Name the blood parasite species.
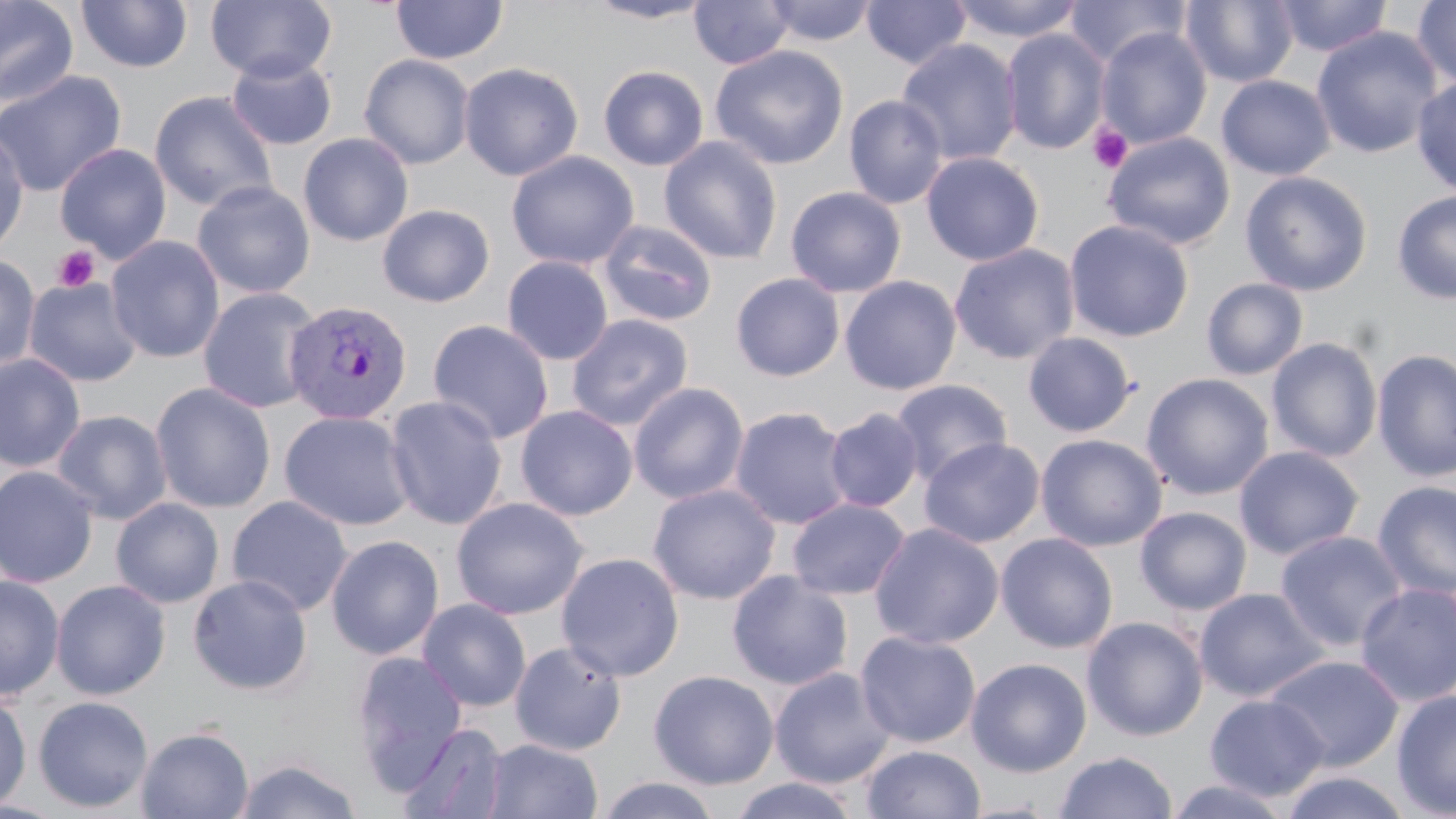

Plasmodium vivax.

Approximate bounding boxes as [x1, y1, x2, y2] in pixels. Platelet locations: [1088, 123, 1134, 173], [52, 245, 99, 292]. Uninfected red blood cell locations: [0, 0, 79, 108], [76, 0, 193, 73], [205, 0, 337, 83], [689, 0, 793, 70], [763, 0, 877, 46], [861, 0, 971, 70], [948, 0, 1086, 44], [1063, 0, 1192, 68], [1181, 0, 1298, 87], [1272, 0, 1393, 58], [1412, 0, 1456, 91], [391, 1, 508, 65], [582, 1, 715, 24], [1096, 26, 1212, 150], [1311, 27, 1443, 160], [1001, 28, 1111, 155], [896, 39, 1023, 166], [709, 45, 849, 170], [226, 52, 338, 150], [358, 53, 475, 170], [458, 61, 584, 181], [598, 64, 709, 171], [0, 70, 127, 198], [1216, 74, 1336, 180], [1411, 76, 1456, 197], [148, 90, 278, 212], [843, 94, 948, 209], [0, 125, 30, 259], [298, 132, 414, 246], [1103, 132, 1236, 251], [659, 136, 783, 265], [54, 143, 172, 263], [506, 150, 639, 270], [920, 151, 1045, 266], [1240, 170, 1374, 296], [192, 180, 315, 299], [785, 186, 907, 298], [1392, 190, 1456, 304], [376, 204, 495, 308], [598, 219, 718, 327], [1063, 219, 1194, 342], [105, 235, 225, 363], [948, 242, 1080, 365], [0, 253, 41, 373], [502, 256, 614, 365], [730, 273, 845, 382], [839, 275, 962, 396], [23, 277, 143, 387], [1200, 278, 1309, 380], [197, 287, 323, 414], [566, 313, 694, 431], [427, 319, 554, 444], [1022, 332, 1138, 438], [1266, 336, 1383, 463], [1372, 349, 1456, 482], [0, 353, 85, 473], [1140, 373, 1275, 500], [890, 378, 1014, 485], [150, 382, 276, 513], [629, 382, 749, 504], [384, 395, 508, 530], [515, 404, 638, 520], [729, 406, 854, 530], [823, 407, 924, 513], [51, 409, 172, 525], [278, 410, 416, 530], [1035, 433, 1168, 552], [919, 437, 1045, 548], [1233, 445, 1365, 560], [0, 465, 99, 588], [1372, 480, 1456, 599], [647, 483, 781, 605], [227, 495, 353, 616], [451, 496, 588, 619], [111, 497, 224, 608], [787, 497, 911, 600], [1135, 506, 1252, 615], [869, 522, 1004, 649], [1275, 530, 1409, 652], [995, 532, 1118, 654], [325, 535, 445, 660], [556, 551, 685, 681], [726, 570, 854, 690], [0, 574, 65, 701], [187, 574, 313, 695], [50, 579, 171, 700], [1354, 582, 1456, 707], [1194, 587, 1329, 702], [417, 598, 532, 711], [1082, 616, 1208, 741], [855, 630, 981, 748], [509, 641, 627, 756], [351, 651, 468, 789], [1263, 654, 1405, 770], [966, 658, 1092, 777], [769, 667, 895, 789], [648, 669, 779, 790], [1391, 689, 1456, 818], [0, 692, 31, 814], [1204, 694, 1329, 801], [32, 696, 154, 813], [398, 722, 509, 818], [136, 726, 253, 819], [481, 738, 602, 819], [861, 744, 986, 819], [1054, 751, 1177, 818], [232, 756, 363, 819], [1278, 770, 1414, 819], [595, 775, 723, 818], [728, 777, 863, 818], [1164, 777, 1293, 818]. Plasmodium vivax-infected red blood cell locations: [282, 298, 413, 425]. Single field of view. Light microscopy. 1000x magnification. May-Grünwald-Giemsa stain. Image is 1456×819 pixels. Thin blood film.